Locate every Plasmodium falciparum parasite and give its life-cycle stage, and locate every leukocyte and any debris.
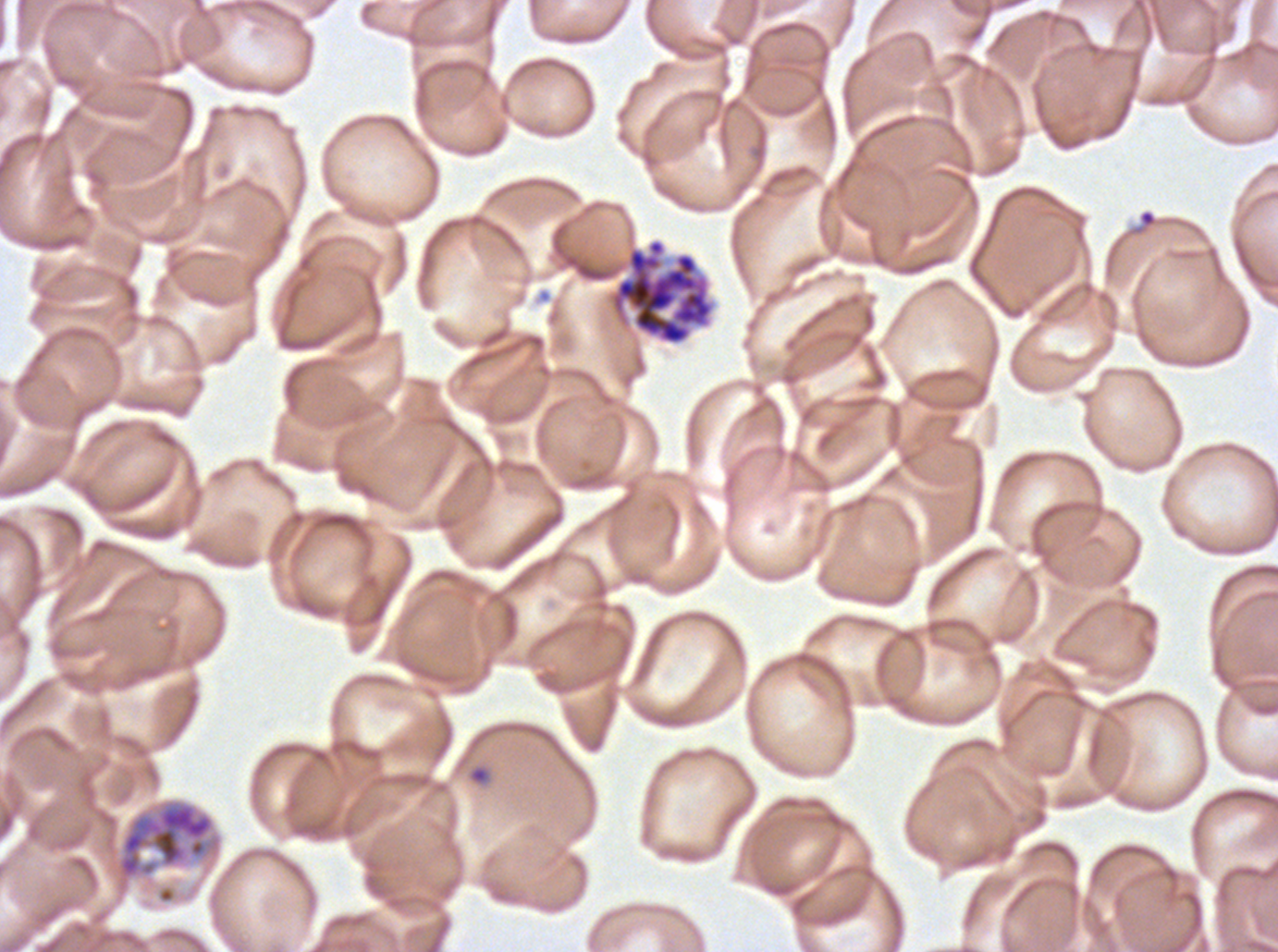

Approximate bounding boxes as {x1, y1, x2, y2} in pixels.
Rings: {1138, 209, 1156, 227}, {467, 763, 491, 786}.
Late schizonts: {114, 798, 223, 895}.
Segmenters: {608, 238, 716, 346}.
No late-ring/early-trophozoite forms, mid trophozoites, late trophozoites, early schizonts, gametocytes, leukocytes, or debris observed.

{
  "stain": "Giemsa",
  "specimen": "Plasmodium falciparum cultured ex vivo for 24 to 48 hours, from a patient in The Gambia",
  "preparation": "thin blood smear",
  "life_cycle_stages_observed": "ring, late schizont, segmenter",
  "field_of_view": "sub-image separated from a larger composite",
  "image_size": "1278×952 pixels"
}